Give the position of every leukocyte visible.
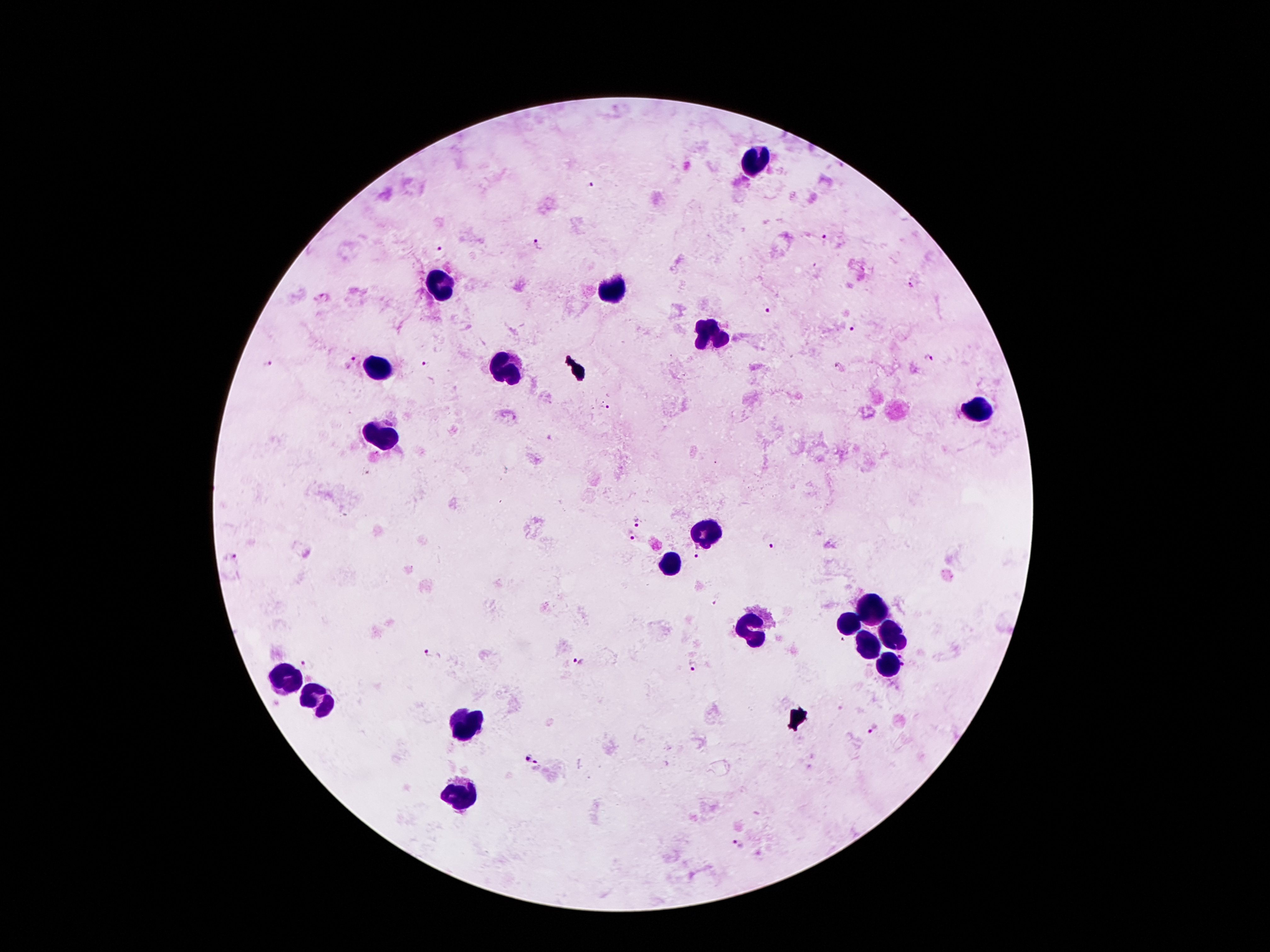
Approximate centers as {x, y} in pixels.
Leukocytes: {754, 164}, {442, 286}, {608, 290}, {711, 335}, {378, 366}, {508, 370}, {976, 411}, {386, 436}, {709, 533}, {671, 563}, {871, 609}, {849, 623}, {748, 626}, {898, 634}, {870, 645}, {889, 667}, {285, 677}, {323, 698}, {467, 724}, {461, 794}.

Malaria parasite locations: {591, 184}, {826, 237}, {537, 243}, {441, 250}, {324, 297}, {768, 310}, {851, 329}, {928, 359}, {351, 360}, {424, 365}, {839, 368}, {638, 521}, {631, 536}, {772, 548}, {695, 556}, {232, 559}, {426, 651}, {576, 662}, {305, 666}, {695, 667}, {875, 729}, {528, 759}, {538, 765}, {738, 843}. Giemsa-stained preparation. Photographed through the microscope eyepiece with a smartphone camera. Single field of view. Image is 1270×952 pixels. Thick peripheral-blood smear. 100x magnification. Patient malaria status: positive for Plasmodium falciparum.